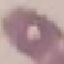

Result: negative for malaria parasites. Acquired by smartphone through the microscope eyepiece. Thin smear of blood. Automatically extracted cell patch, resized to 64 × 64 pixels. Giemsa-stained preparation.